Give the position of each P. falciparum parasite with its life-cycle stage, each leukocyte, and any debris.
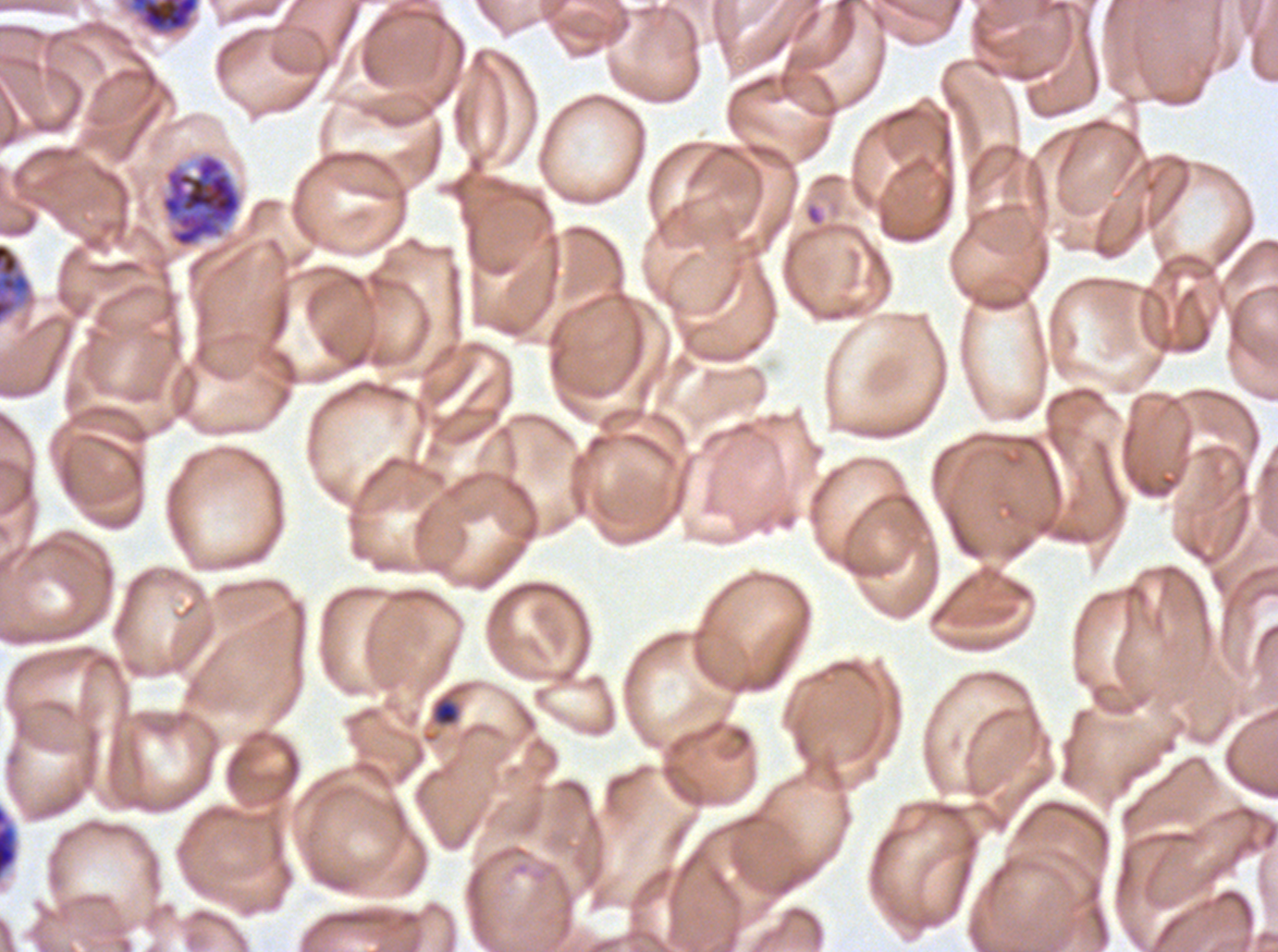
Approximate bounding boxes as [x1, y1, x2, y2] in pixels.
Late-ring/early-trophozoite forms: [435, 701, 458, 725].
Early schizonts: [129, 0, 200, 33], [158, 152, 244, 250], [0, 242, 33, 323].
Late schizonts: [0, 806, 18, 876].
No rings, mid trophozoites, late trophozoites, segmenters, gametocytes, leukocytes, or debris observed.

Giemsa-stained preparation. P. falciparum from a patient in The Gambia, cultured ex vivo for 24 to 48 hours. A sub-image separated from a larger composite. Image is 1278×952 pixels. Thin blood smear. Life-cycle stages observed: late-ring/early-trophozoite, early schizont, late schizont.